Report the malaria status of this cell.
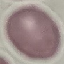

It is uninfected.

{
  "image_type": "automatically extracted cell patch, resized to 64 × 64 pixels",
  "capture": "smartphone camera at the microscope eyepiece",
  "preparation": "thin blood smear",
  "stain": "Giemsa"
}